Report the malaria status of this cell.
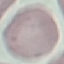
Uninfected.

Thin blood smear. Cell patch, automatically extracted from a larger field of view and resized to 64 × 64 pixels. Giemsa-stained preparation. Acquired by smartphone through the microscope eyepiece.